Identify the cell.
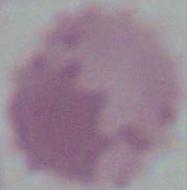

This is an erythrocyte.

magnification = 1000x
modality = photomicrograph